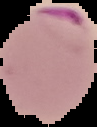
preparation = thin blood film
malaria status = parasitized
image type = cell region segmented out of the field of view; surrounding area masked to black
image size = 97×127 pixels